Assess this cell for malaria.
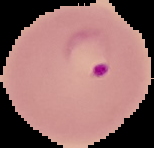
Parasitized.

Summary:
  - Preparation: thin blood film
  - Image type: segmented cell region with the area outside set to black
  - Image size: 154×148 pixels